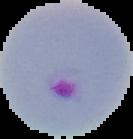
Cell region segmented out of the field of view; the surrounding area is masked to black. Image is 133×139 pixels. From a thin blood smear. Result: malaria parasites detected.